Identify the parasite.
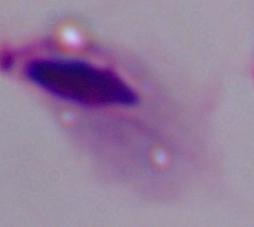
This is a trichomonad.

Photomicrograph. Captured at 1000x magnification.